Locate every blood parasite and identify its species.
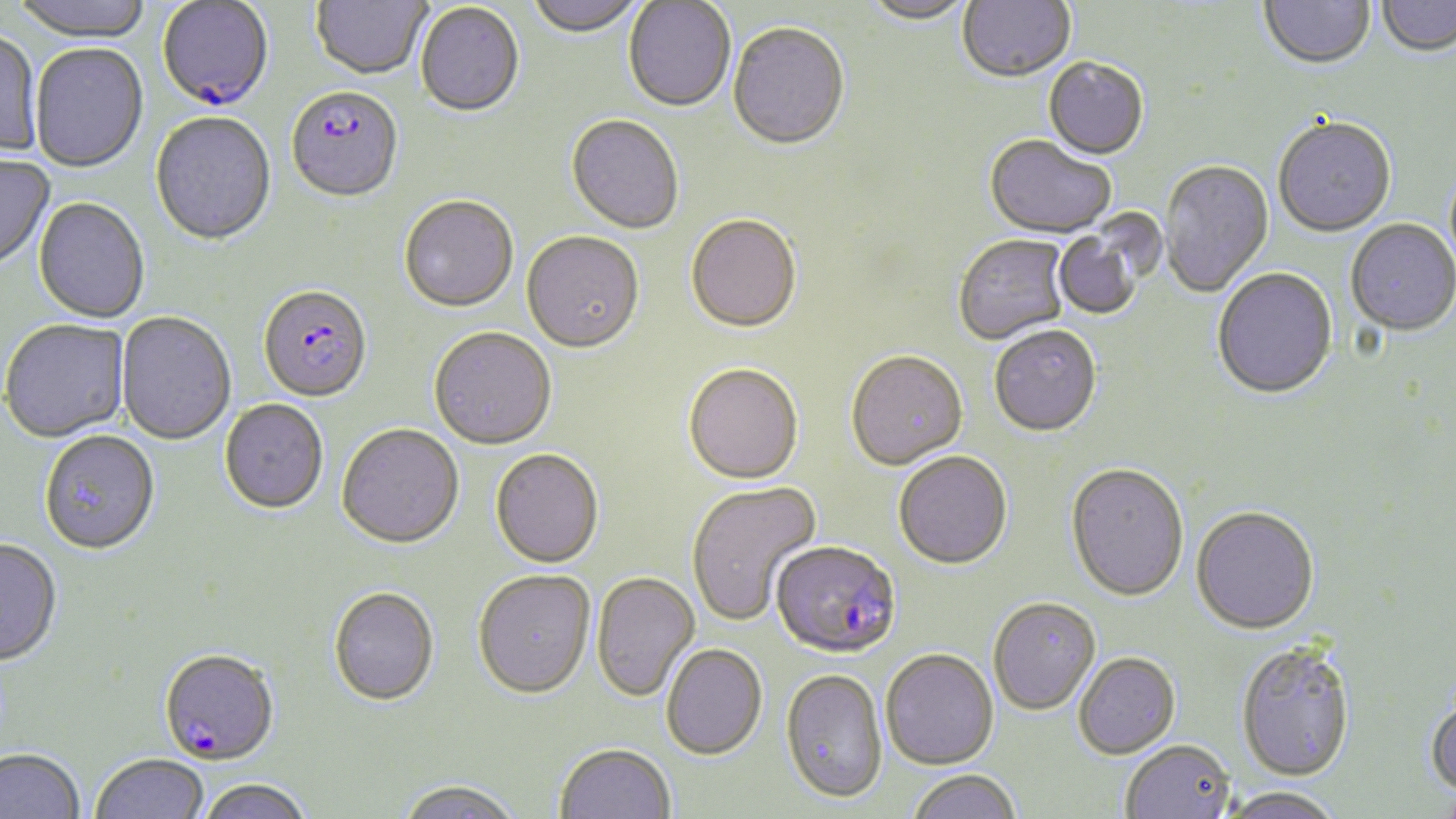

Approximate bounding boxes as [x1, y1, x2, y2] in pixels.
Plasmodium falciparum-infected red blood cells: [156, 2, 275, 113], [286, 89, 404, 206], [258, 287, 373, 404], [771, 543, 902, 661], [158, 652, 279, 768].
No Plasmodium ovale, Plasmodium malariae, Plasmodium vivax, Babesia divergens, or Trypanosoma brucei observed.

Summary:
  - Uninfected red blood cell locations: [8, 0, 154, 44], [311, 0, 432, 82], [525, 0, 645, 39], [858, 0, 977, 27], [958, 0, 1075, 85], [1259, 0, 1375, 73], [623, 1, 736, 114], [1376, 1, 1456, 59], [415, 4, 525, 119], [727, 25, 851, 153], [0, 31, 43, 162], [29, 44, 149, 174], [1043, 59, 1149, 162], [150, 114, 277, 247], [565, 116, 683, 236], [1273, 119, 1396, 239], [984, 137, 1116, 241], [0, 155, 56, 272], [1159, 161, 1274, 298], [399, 197, 518, 314], [33, 199, 150, 324], [686, 217, 802, 336], [1052, 218, 1152, 321], [1346, 220, 1456, 339], [521, 233, 645, 356], [954, 235, 1070, 346], [1212, 270, 1338, 403], [116, 313, 236, 446], [1, 321, 130, 444], [990, 327, 1102, 440], [429, 329, 556, 451], [845, 353, 969, 473], [683, 366, 804, 487], [219, 400, 328, 515], [335, 426, 464, 551], [39, 433, 160, 557], [490, 450, 604, 569], [894, 453, 1013, 572], [1065, 465, 1189, 605], [686, 481, 822, 627], [1191, 509, 1320, 638], [0, 540, 62, 669], [473, 571, 596, 701], [591, 573, 700, 703], [329, 587, 439, 707], [988, 599, 1101, 718], [1237, 645, 1357, 785], [661, 646, 767, 762], [881, 651, 999, 772], [1074, 655, 1181, 761], [780, 670, 887, 806], [1425, 694, 1456, 800], [1120, 743, 1235, 819], [554, 746, 676, 818], [0, 749, 85, 819], [91, 754, 209, 819], [908, 771, 1022, 819], [199, 779, 313, 819], [394, 780, 524, 819], [1435, 784, 1455, 819], [1218, 788, 1344, 819]
  - Slide-level diagnosis: Plasmodium falciparum
  - Modality: optical microscopy
  - Magnification: 1000x
  - Stain: May-Grünwald-Giemsa
  - Image size: 1456×819 pixels
  - Preparation: thin blood smear
  - Field of view: single